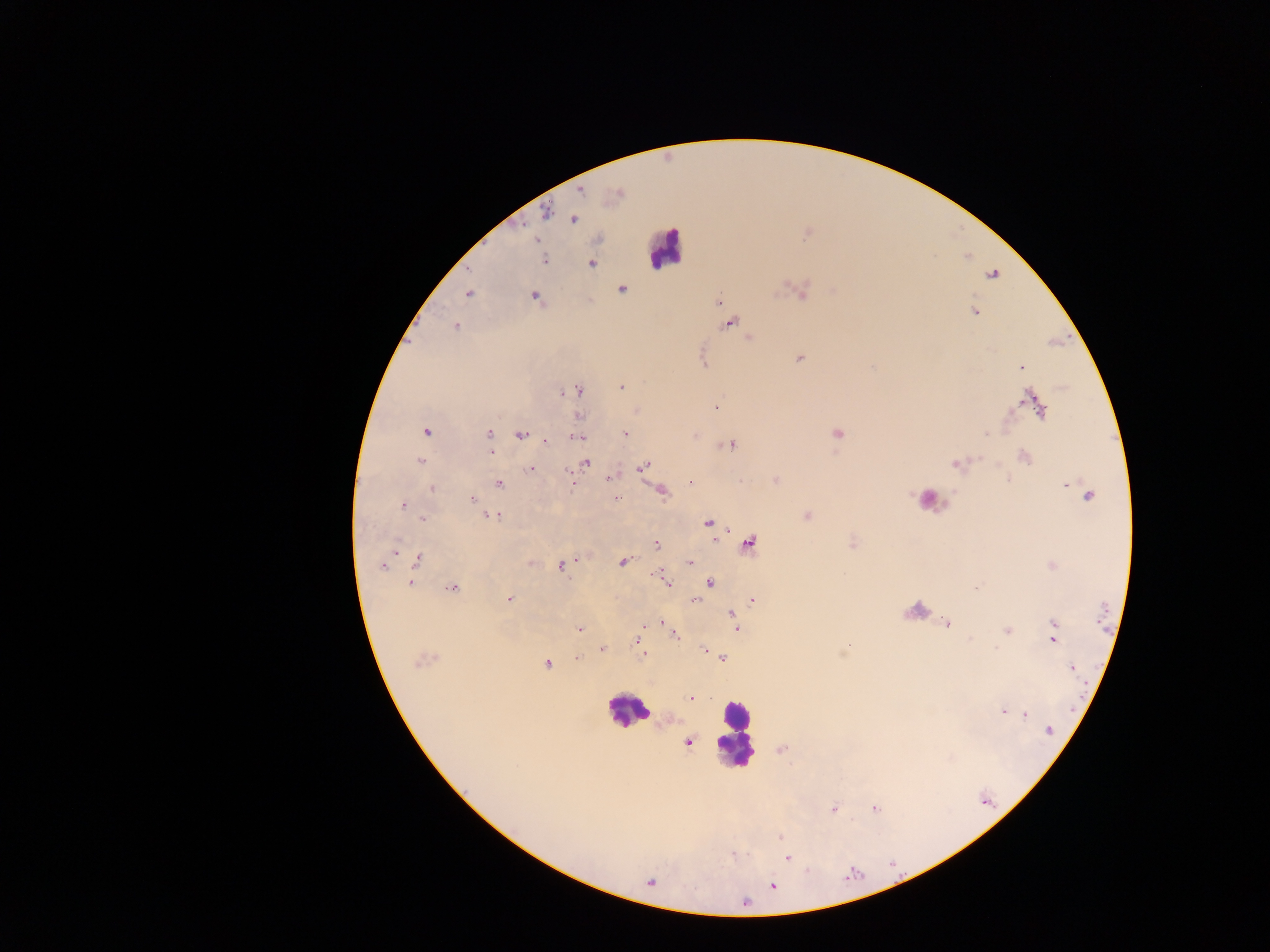
country = Ghana
Plasmodium parasite locations = approximate centers as [x, y] in pixels: [580, 190], [617, 194], [547, 213], [572, 218], [536, 240], [544, 260], [591, 263], [992, 274], [622, 289], [801, 291], [468, 293], [535, 296], [719, 302], [973, 311], [728, 322], [455, 326], [749, 337], [799, 359], [1021, 367], [620, 386], [577, 390], [1034, 402], [716, 407], [637, 410], [578, 415], [425, 430], [624, 433], [837, 433], [488, 434], [520, 434], [695, 434], [579, 437], [544, 441], [730, 445], [491, 451], [1023, 456], [420, 460], [957, 462], [585, 463], [642, 467], [530, 469], [612, 476], [1008, 479], [572, 480], [774, 480], [691, 482], [498, 483], [1067, 484], [431, 488], [662, 491], [1089, 495], [471, 499], [614, 499], [401, 504], [490, 515], [806, 515], [422, 519], [708, 522], [748, 542], [853, 542], [656, 545], [394, 548], [417, 559], [622, 561], [531, 562], [690, 562], [383, 565], [561, 565], [1051, 565], [658, 574], [409, 582], [710, 582], [666, 583], [453, 587], [509, 599], [752, 599], [695, 600], [733, 616], [662, 623], [947, 623], [1054, 623], [666, 624], [579, 628], [736, 629], [1006, 630], [674, 633], [971, 638], [638, 639], [1052, 640], [848, 646], [642, 647], [602, 648], [702, 649], [644, 655], [575, 657], [722, 657], [422, 659], [547, 663], [1073, 667], [690, 697], [1002, 711], [1025, 714], [1048, 730], [687, 741], [781, 749], [874, 807], [833, 808], [780, 836], [787, 857], [649, 882], [772, 886]
field of view = single
preparation = thick blood film
image size = 1270×952 pixels
capture = mobile-phone photograph through a microscope
leukocyte locations = approximate centers as [x, y] in pixels: [665, 248], [928, 499], [627, 709], [733, 735]